Mark where platelets are.
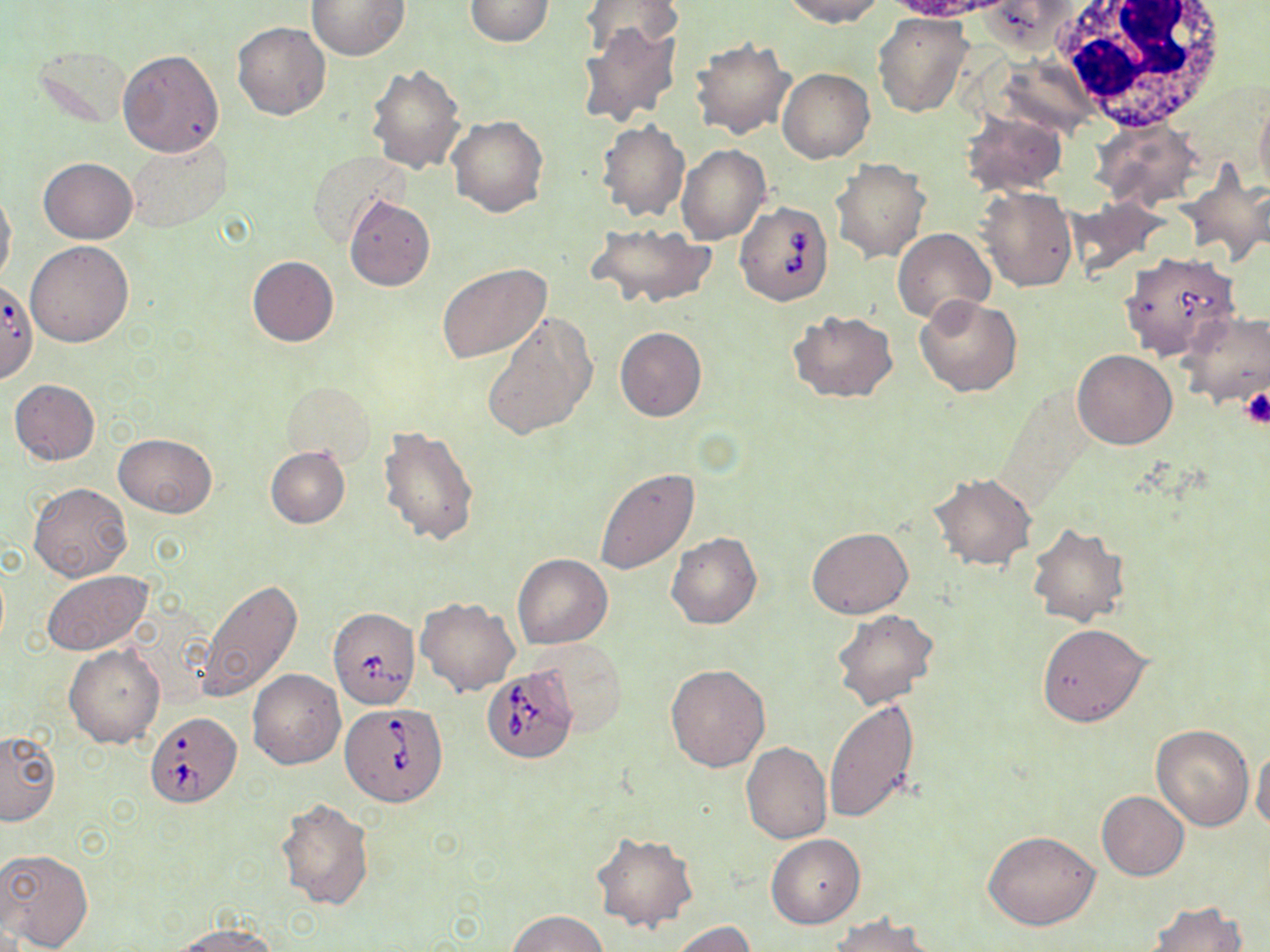

Approximate bounding boxes as (x1,y1)-(x2,y2) corner pairs in pixels.
Platelets: (1240,388)-(1269,430).

Summary:
  - White blood cell locations: (1048,0)-(1232,129)
  - Babesia divergens-infected red blood cell locations: (734,200)-(833,305), (1119,251)-(1240,360), (0,284)-(37,390), (327,607)-(420,709), (482,667)-(578,765), (341,702)-(447,805), (146,711)-(241,806)
  - Uninfected red blood cell locations: (306,0)-(409,59), (465,0)-(554,46), (579,0)-(683,62), (780,0)-(887,27), (978,1)-(1080,54), (873,12)-(973,117), (233,22)-(330,120), (578,23)-(681,126), (689,38)-(795,140), (36,48)-(131,128), (118,49)-(224,158), (367,63)-(466,174), (777,68)-(874,163), (1254,93)-(1270,201), (960,109)-(1066,197), (447,115)-(549,218), (1091,118)-(1203,209), (596,119)-(690,221), (128,135)-(233,232), (676,145)-(771,246), (307,149)-(407,247), (39,157)-(137,244), (831,159)-(931,263), (1179,166)-(1270,268), (974,186)-(1078,292), (0,188)-(17,287), (343,195)-(435,290), (589,223)-(716,309), (893,228)-(995,323), (26,240)-(135,347), (246,256)-(338,347), (437,263)-(551,363), (914,295)-(1022,397), (789,310)-(898,403), (1178,311)-(1270,408), (482,312)-(596,442), (615,326)-(707,421), (1072,349)-(1177,450), (8,379)-(99,465), (282,381)-(375,462), (377,425)-(482,546), (113,433)-(217,517), (264,447)-(351,528), (594,466)-(700,575), (927,473)-(1037,570), (28,483)-(133,583), (1025,522)-(1130,628), (807,526)-(913,619), (666,532)-(763,630), (512,553)-(612,649), (41,569)-(154,657), (197,577)-(302,704), (417,596)-(521,696), (831,609)-(938,711), (1037,622)-(1150,727), (531,638)-(629,735), (64,644)-(165,748), (665,664)-(770,771), (248,669)-(345,768), (825,699)-(920,823), (1150,723)-(1254,830), (0,732)-(60,826), (740,742)-(832,845), (1252,746)-(1270,833), (1097,791)-(1188,881), (276,796)-(375,910), (983,831)-(1100,930), (591,832)-(697,933), (766,834)-(864,929), (0,848)-(94,951), (1145,901)-(1247,952), (507,910)-(610,952), (830,914)-(936,952), (169,920)-(280,950), (671,921)-(755,952)
  - Slide-level diagnosis: Babesia divergens
  - Image size: 1270×952 pixels
  - Modality: light microscopy
  - Magnification: 1000x
  - Preparation: thin blood film
  - Field of view: single
  - Stain: May-Grünwald-Giemsa